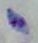
Captured at 1000x magnification. Toxoplasma gondii is seen. Photomicrograph.